Comment on the morphology of the red blood cells.
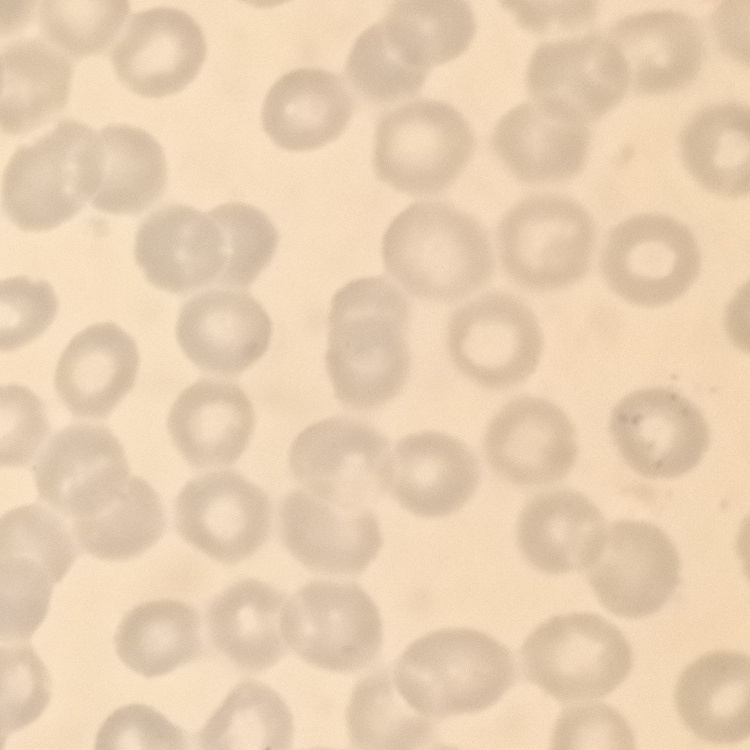
No rouleaux formation.

image type = square crop of a larger photomicrograph
stain = Field's or Giemsa
preparation = thin blood smear